Assess this cell for malaria.
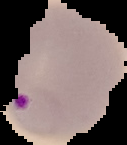

It is parasitized.

Summary:
  - Preparation: thin blood smear
  - Image size: 127×145 pixels
  - Image type: cell region segmented out of the field of view; surrounding area masked to black